Report the malaria status of this cell.
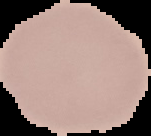
Uninfected.

preparation = thin blood smear
image type = segmented cell region on a black background
image size = 151×136 pixels